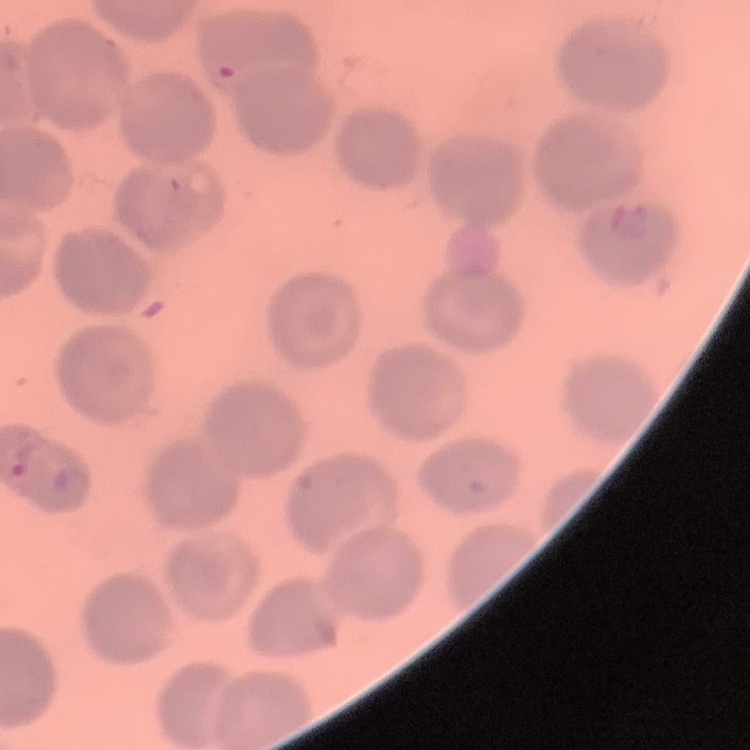

The red blood cells show no rouleaux formation. One tile cut from a larger photomicrograph. Stained with either Field's or Giemsa. Thin blood smear.